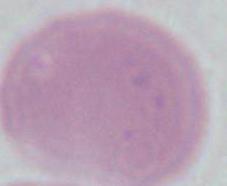

{
  "magnification": "1000x",
  "modality": "photomicrograph",
  "identification": "erythrocyte"
}